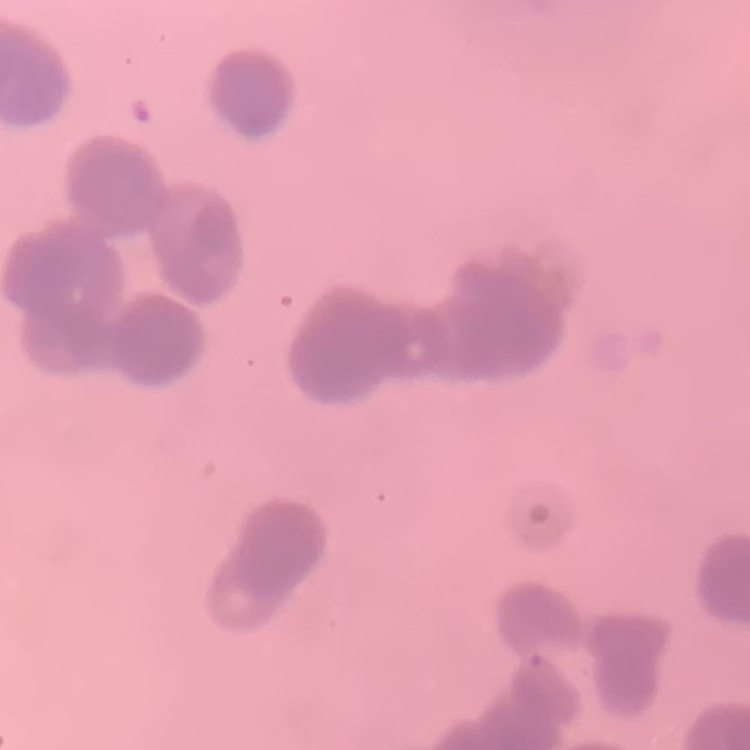

The erythrocytes show rouleaux formation. One tile cut from a larger photomicrograph. Field's or Giemsa stain. Thin blood smear.